Name the blood parasite species.
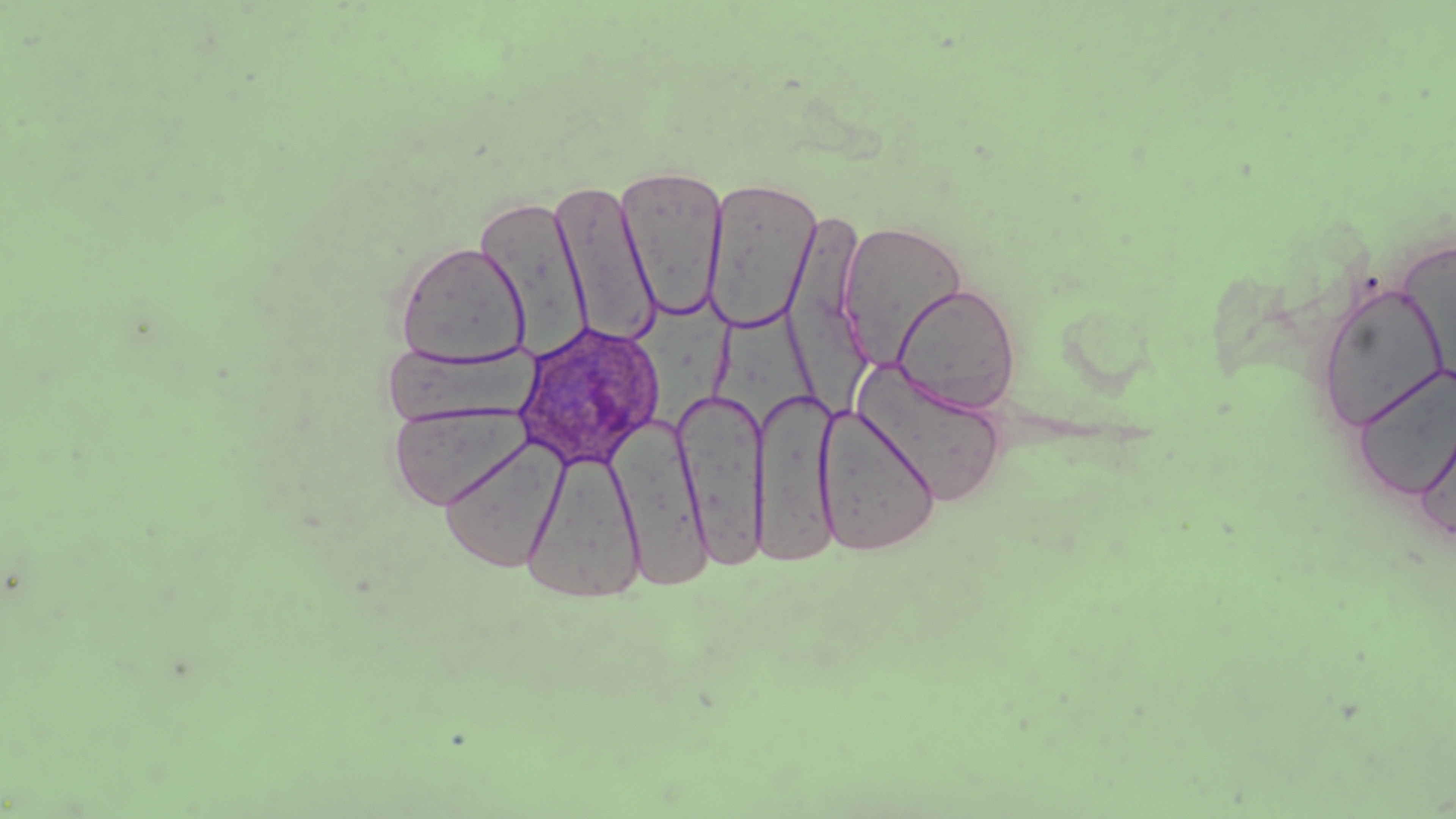

Plasmodium ovale.

Summary:
  - Coordinate format: approximate bounding boxes as named x1/y1/x2/y2 corners in pixels
  - Uninfected red blood cell locations: (x1=616, y1=166, x2=729, y2=321), (x1=703, y1=177, x2=821, y2=334), (x1=549, y1=180, x2=661, y2=348), (x1=474, y1=192, x2=591, y2=354), (x1=785, y1=204, x2=868, y2=403), (x1=837, y1=220, x2=969, y2=369), (x1=395, y1=241, x2=530, y2=367), (x1=1314, y1=281, x2=1452, y2=433), (x1=891, y1=282, x2=1021, y2=413), (x1=638, y1=302, x2=740, y2=428), (x1=719, y1=314, x2=820, y2=424), (x1=381, y1=341, x2=537, y2=426), (x1=852, y1=361, x2=1008, y2=507), (x1=1354, y1=365, x2=1456, y2=501), (x1=752, y1=388, x2=841, y2=565), (x1=674, y1=389, x2=767, y2=570), (x1=387, y1=403, x2=530, y2=511), (x1=814, y1=403, x2=941, y2=556), (x1=1413, y1=410, x2=1456, y2=546), (x1=612, y1=416, x2=712, y2=590), (x1=440, y1=436, x2=567, y2=573), (x1=522, y1=449, x2=645, y2=604)
  - Plasmodium ovale-infected red blood cell locations: (x1=513, y1=320, x2=664, y2=470)
  - Field of view: one of a larger specimen
  - Magnification: 1000x
  - Image size: 1456×819 pixels
  - Preparation: thin blood smear
  - Stain: May-Grünwald-Giemsa
  - Modality: optical microscopy